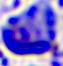 400x magnification. A leukocyte is seen. Micrograph.